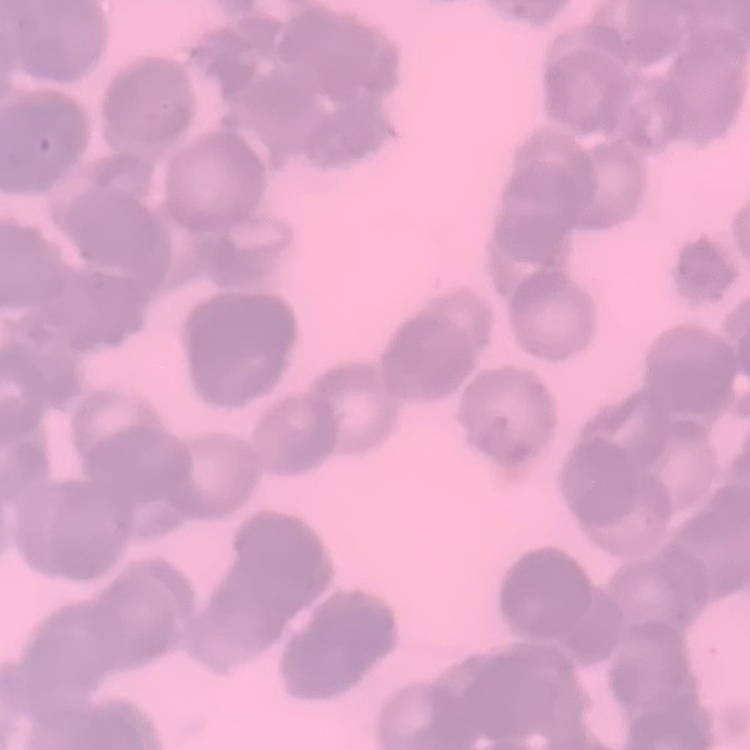
red blood cell morphology = rouleaux formation
image type = one tile cut from a larger photomicrograph
preparation = thin blood smear
stain = Field's or Giemsa